Identify the cell.
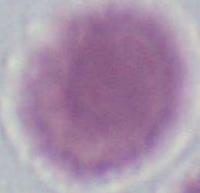

An erythrocyte.

Captured at 1000x magnification. Micrograph.